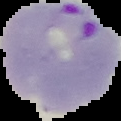

Summary:
  - Result: malaria parasites identified
  - Image type: segmented cell region on a black background
  - Preparation: thin blood film
  - Image size: 121×121 pixels